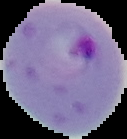

Summary:
  - Preparation: thin blood smear
  - Image type: segmented cell region with the area outside set to black
  - Image size: 127×139 pixels
  - Malaria status: parasitized